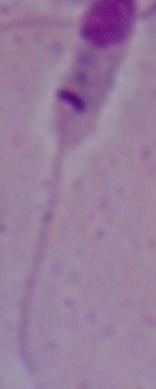
1000x magnification. Micrograph. A Leishmania parasite is seen.